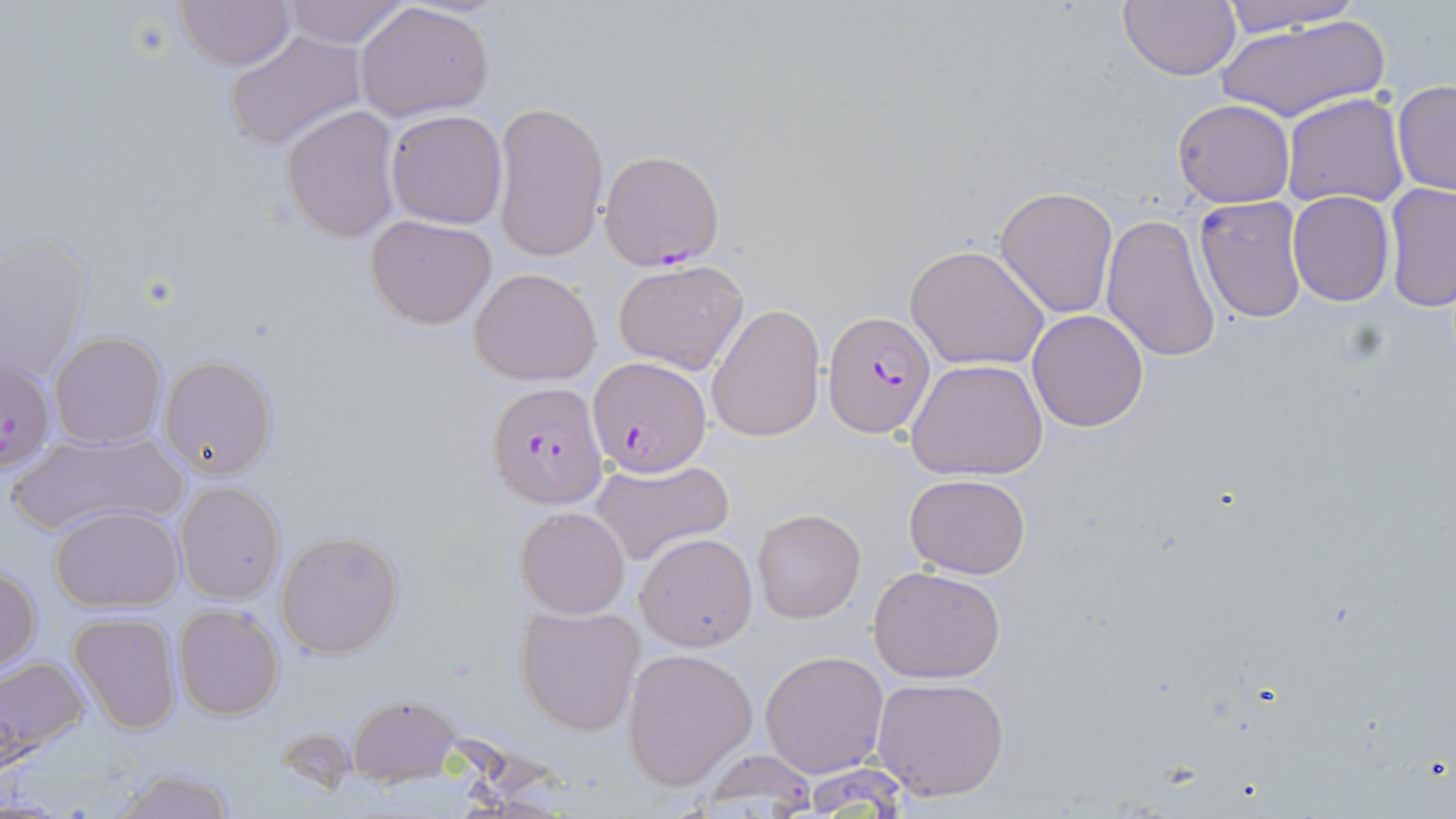

Summary:
  - Coordinate format: approximate bounding boxes as (x1, y1, x2, y2) in pixels
  - Plasmodium falciparum-infected red blood cell locations: (598, 149, 725, 270), (824, 311, 935, 438), (2, 358, 55, 472), (588, 358, 710, 474), (490, 381, 608, 511)
  - Uninfected red blood cell locations: (174, 0, 293, 69), (277, 0, 412, 46), (1118, 0, 1239, 82), (1217, 0, 1368, 34), (355, 2, 494, 121), (1213, 11, 1391, 125), (223, 31, 368, 151), (1391, 81, 1455, 197), (1281, 93, 1408, 209), (1173, 98, 1295, 207), (494, 101, 609, 265), (280, 105, 400, 242), (385, 109, 507, 227), (1382, 183, 1456, 312), (995, 186, 1119, 318), (1287, 191, 1395, 307), (1193, 197, 1308, 323), (365, 213, 498, 329), (1100, 214, 1221, 363), (1, 232, 91, 381), (906, 243, 1050, 370), (611, 259, 749, 375), (469, 267, 602, 384), (706, 304, 826, 443), (1027, 309, 1149, 431), (49, 331, 167, 451), (157, 355, 278, 480), (907, 358, 1048, 481), (7, 432, 187, 536), (590, 457, 735, 568), (904, 472, 1030, 579), (174, 480, 285, 603), (50, 505, 185, 612), (515, 506, 629, 618), (752, 506, 866, 624), (275, 528, 404, 659), (635, 531, 758, 651), (868, 565, 1007, 682), (0, 566, 41, 672), (173, 604, 285, 720), (516, 606, 643, 735), (67, 612, 181, 734), (622, 648, 758, 790), (760, 650, 889, 777), (0, 656, 88, 757), (871, 677, 1010, 801), (349, 694, 459, 783), (697, 748, 821, 811), (111, 766, 239, 819)
  - Slide-level diagnosis: Plasmodium falciparum
  - Field of view: one of a larger specimen
  - Modality: optical microscopy
  - Preparation: thin blood smear
  - Stain: May-Grünwald-Giemsa
  - Magnification: 1000x
  - Image size: 1456×819 pixels